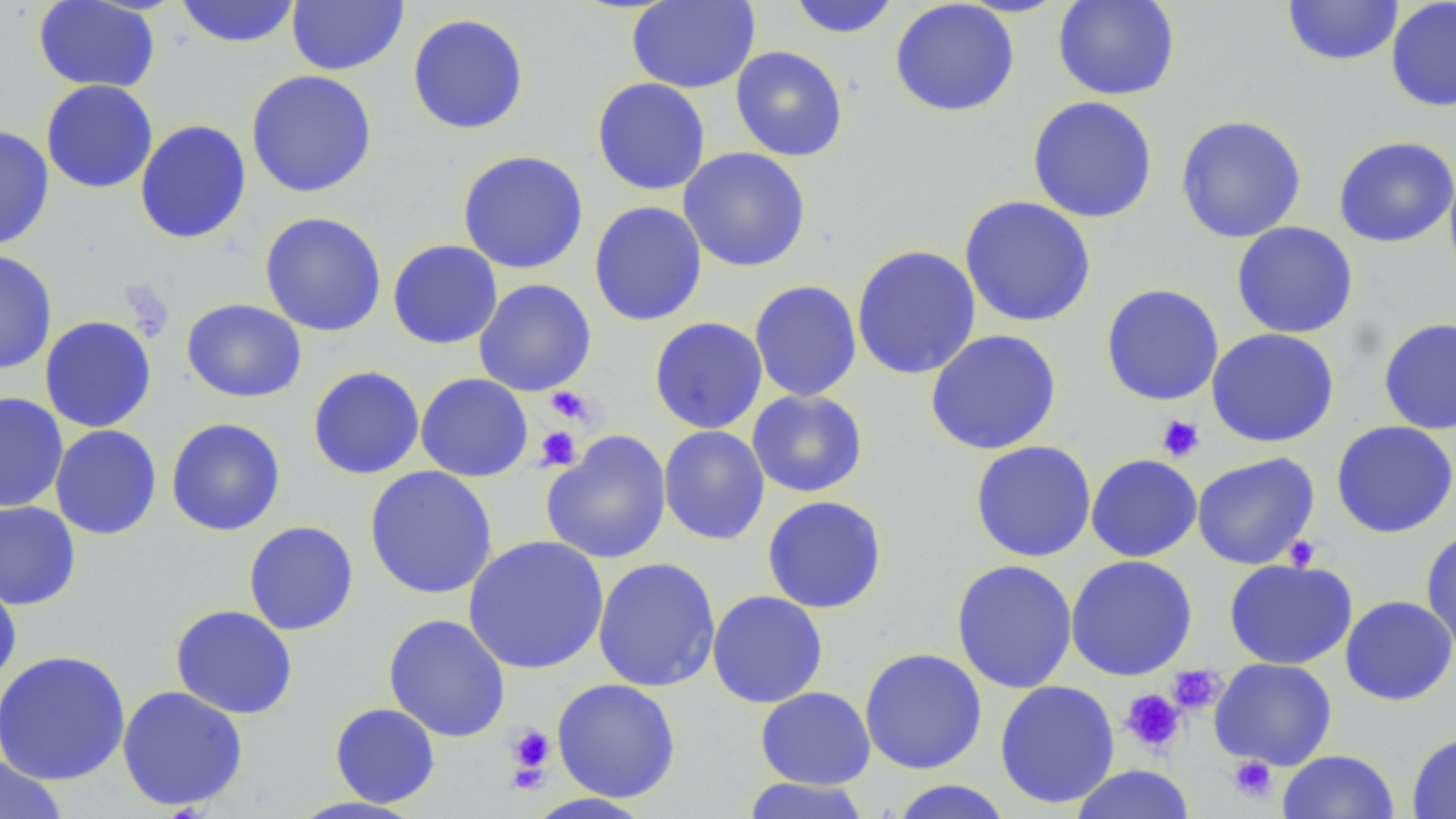

Approximate bounding boxes as (x1, y1, x2, y2) in pixels. Platelet locations: (545, 386, 595, 426), (1157, 414, 1205, 462), (535, 426, 581, 471), (1284, 534, 1322, 571), (1167, 664, 1225, 715), (1120, 689, 1186, 755), (506, 724, 555, 780), (1227, 756, 1277, 803). Uninfected red blood cell locations: (33, 0, 160, 93), (174, 0, 302, 48), (286, 0, 409, 75), (787, 0, 901, 39), (890, 0, 1020, 117), (1052, 0, 1181, 101), (1282, 0, 1403, 66), (626, 1, 760, 93), (1385, 1, 1456, 112), (407, 13, 529, 135), (730, 45, 848, 161), (245, 70, 378, 198), (591, 77, 711, 196), (40, 80, 158, 194), (1027, 96, 1158, 223), (1175, 114, 1307, 243), (134, 120, 251, 245), (0, 125, 54, 250), (1333, 136, 1456, 248), (678, 147, 811, 272), (457, 150, 589, 274), (1444, 163, 1456, 285), (959, 195, 1096, 328), (588, 200, 708, 327), (259, 211, 387, 337), (1231, 222, 1359, 339), (387, 239, 503, 349), (851, 244, 982, 380), (0, 250, 57, 375), (473, 278, 597, 396), (749, 279, 862, 402), (1100, 283, 1224, 406), (181, 298, 306, 403), (39, 315, 157, 433), (648, 316, 768, 434), (1378, 317, 1456, 435), (1206, 328, 1339, 448), (924, 329, 1062, 455), (307, 365, 424, 480), (415, 373, 533, 481), (746, 389, 868, 498), (0, 392, 69, 513), (166, 417, 286, 536), (1330, 420, 1456, 538), (50, 424, 162, 540), (658, 425, 770, 546), (541, 430, 672, 565), (969, 440, 1097, 562), (1191, 452, 1320, 570), (1086, 453, 1202, 562), (364, 466, 498, 599), (761, 495, 888, 614), (0, 500, 82, 610), (243, 520, 359, 636), (1420, 527, 1456, 655), (462, 534, 609, 675), (1065, 554, 1198, 681), (592, 557, 721, 692), (950, 558, 1078, 694), (1224, 558, 1358, 670), (0, 575, 22, 687), (706, 590, 828, 708), (1339, 595, 1456, 706), (170, 604, 298, 719), (383, 613, 511, 742), (859, 647, 987, 774), (0, 649, 131, 786), (1209, 657, 1337, 770), (551, 678, 681, 803), (994, 679, 1120, 809), (116, 685, 248, 812), (755, 686, 876, 790), (329, 702, 440, 808), (1406, 732, 1456, 819), (1278, 749, 1399, 819), (0, 756, 69, 819), (1069, 764, 1196, 819), (739, 777, 873, 819), (887, 780, 1015, 819), (522, 793, 655, 818). Slide-level diagnosis: no evidence of blood parasites. Thin blood smear. Captured at 1000x magnification. Image is 1456×819 pixels. May-Grünwald-Giemsa stain. Single field of view. Optical microscopy.